Identify the parasite.
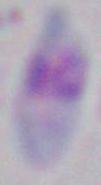
Toxoplasma gondii.

magnification: 1000x
modality: photomicrograph